State which cell type is depicted.
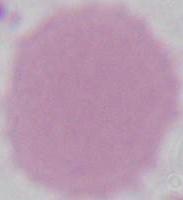

An erythrocyte.

Summary:
  - Modality: photomicrograph
  - Magnification: 1000x